Locate every blood parasite and identify its species.
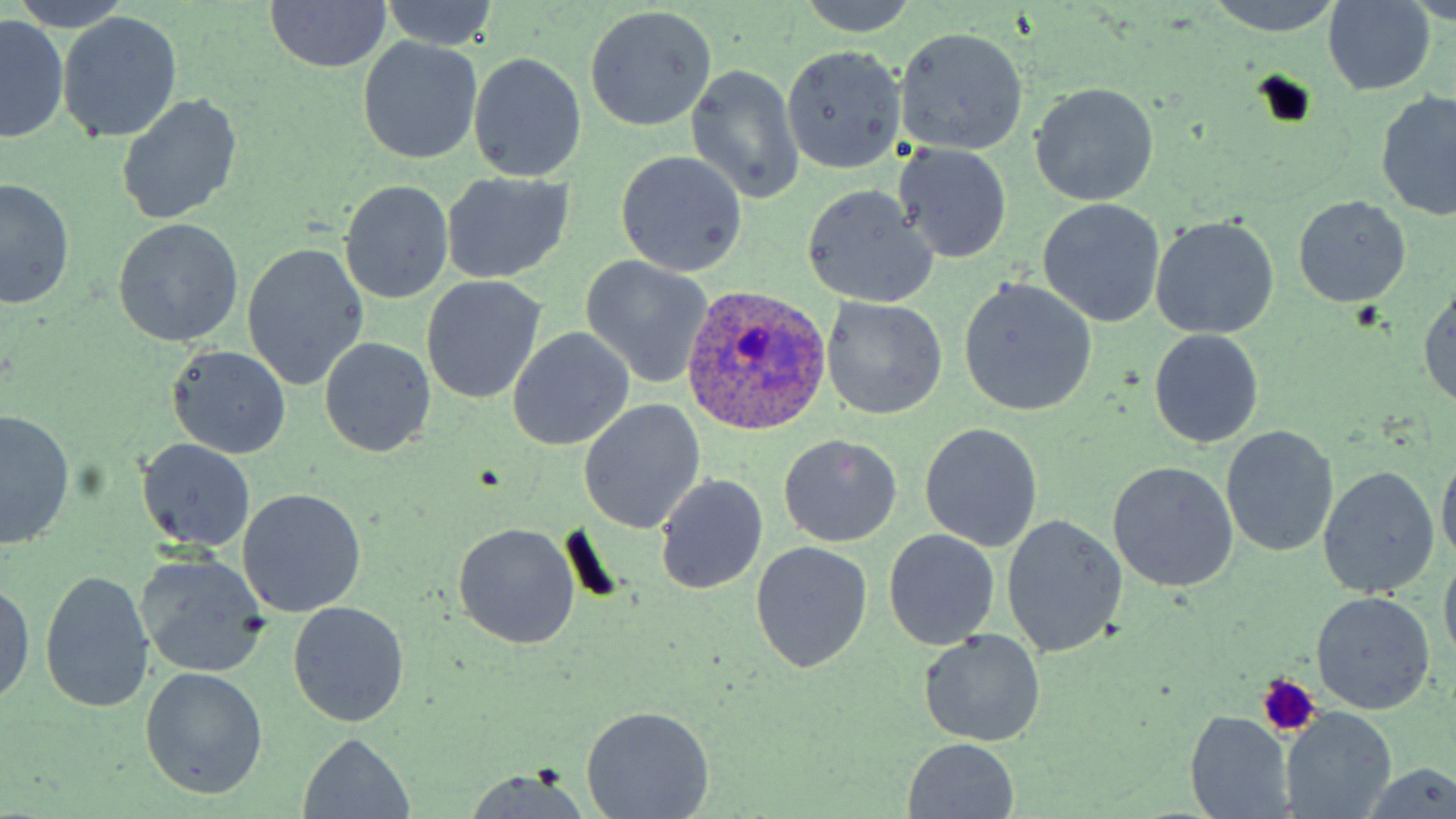

Approximate bounding boxes as [x1, y1, x2, y2] in pixels.
Plasmodium ovale-infected red blood cells: [678, 286, 834, 438].
No Plasmodium falciparum, Plasmodium malariae, Plasmodium vivax, Babesia divergens, or Trypanosoma brucei observed.

slide_level_diagnosis: Plasmodium ovale
image_size: 1456×819 pixels
uninfected_red_blood_cell_locations: 'approximate bounding boxes as [x1, y1, x2, y2] in pixels: [10, 0, 137, 31], [1201, 0, 1346, 35], [264, 1, 392, 73], [1414, 1, 1456, 26], [376, 2, 501, 51], [793, 2, 923, 36], [1321, 2, 1436, 95], [583, 5, 717, 132], [57, 12, 183, 144], [1, 18, 67, 142], [896, 27, 1029, 155], [358, 38, 483, 165], [779, 44, 905, 174], [469, 53, 587, 181], [685, 63, 805, 207], [1030, 83, 1158, 206], [1377, 91, 1456, 221], [115, 94, 245, 226], [895, 145, 1011, 265], [615, 150, 749, 276], [443, 174, 575, 285], [0, 178, 74, 310], [340, 180, 453, 305], [801, 183, 938, 309], [1292, 195, 1410, 310], [1037, 199, 1166, 327], [1151, 215, 1279, 339], [113, 217, 243, 347], [241, 242, 369, 391], [580, 256, 714, 388], [420, 276, 546, 403], [958, 279, 1097, 417], [1417, 283, 1456, 408], [820, 297, 948, 420], [508, 327, 634, 451], [1149, 330, 1263, 448], [318, 337, 437, 458], [165, 344, 292, 460], [579, 400, 705, 534], [0, 412, 76, 549], [920, 422, 1044, 552], [1222, 426, 1337, 557], [778, 434, 902, 547], [135, 437, 258, 553], [1437, 445, 1456, 569], [1107, 461, 1238, 593], [1318, 465, 1440, 599], [655, 473, 769, 596], [236, 489, 366, 617], [1000, 514, 1127, 659], [452, 523, 580, 651], [883, 529, 998, 651], [749, 542, 873, 673], [1439, 550, 1456, 667], [134, 554, 272, 680], [38, 569, 153, 712], [0, 580, 34, 708], [1311, 592, 1435, 714], [288, 601, 410, 727], [920, 629, 1046, 748], [140, 667, 268, 800], [582, 705, 714, 819], [1282, 708, 1396, 818], [1186, 712, 1292, 819], [298, 732, 414, 817], [903, 737, 1020, 818], [1360, 763, 1456, 819], [462, 768, 596, 819]'
stain: May-Grünwald-Giemsa
modality: optical microscopy
field_of_view: single
platelet_locations: 'approximate bounding boxes as [x1, y1, x2, y2] in pixels: [1255, 675, 1320, 737]'
preparation: thin blood film
magnification: 1000x